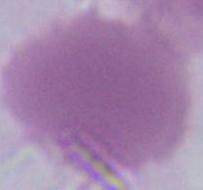 Captured at 1000x magnification. An erythrocyte is shown. Photomicrograph.